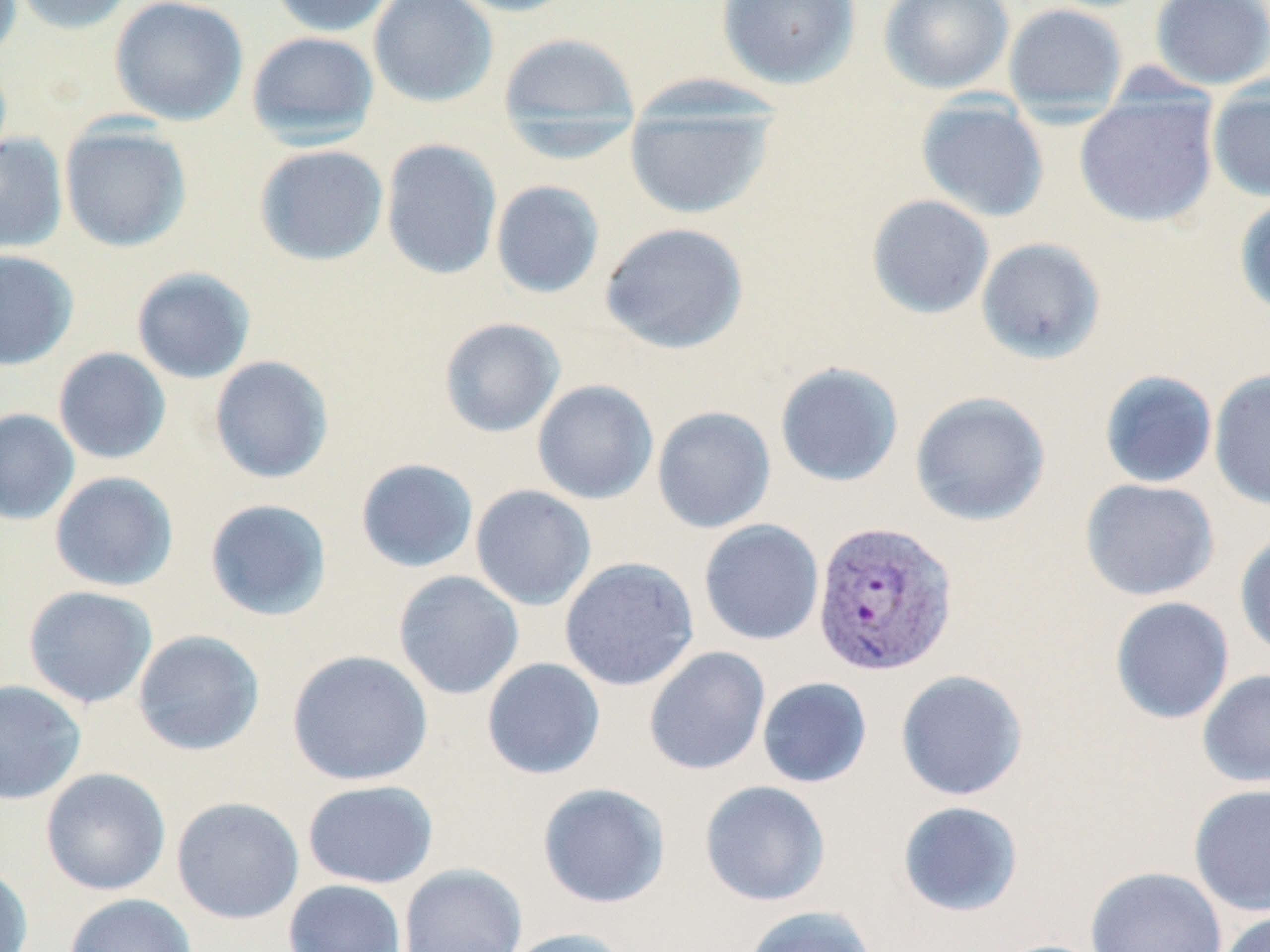

slide_level_diagnosis: Plasmodium vivax
stain: May-Grünwald-Giemsa
plasmodium_vivax_infected_red_blood_cell_locations: 'approximate bounding boxes as named x1/y1/x2/y2 corners in pixels: (x1=810, y1=520, x2=959, y2=676)'
magnification: 1000x
image_size: 1270×952 pixels
preparation: thin blood smear
modality: optical microscopy
field_of_view: single
uninfected_red_blood_cell_locations: 'approximate bounding boxes as named x1/y1/x2/y2 corners in pixels: (x1=10, y1=0, x2=135, y2=34), (x1=109, y1=0, x2=248, y2=126), (x1=268, y1=0, x2=397, y2=37), (x1=368, y1=0, x2=498, y2=108), (x1=444, y1=0, x2=583, y2=17), (x1=716, y1=0, x2=861, y2=89), (x1=878, y1=0, x2=1015, y2=94), (x1=1150, y1=0, x2=1270, y2=90), (x1=1003, y1=3, x2=1128, y2=116), (x1=497, y1=30, x2=640, y2=134), (x1=246, y1=31, x2=380, y2=148), (x1=1207, y1=81, x2=1270, y2=204), (x1=1074, y1=97, x2=1219, y2=228), (x1=915, y1=98, x2=1049, y2=223), (x1=624, y1=102, x2=778, y2=219), (x1=59, y1=122, x2=192, y2=252), (x1=0, y1=133, x2=68, y2=254), (x1=380, y1=138, x2=502, y2=280), (x1=254, y1=144, x2=389, y2=266), (x1=490, y1=180, x2=605, y2=299), (x1=866, y1=194, x2=995, y2=319), (x1=1234, y1=195, x2=1270, y2=318), (x1=599, y1=222, x2=749, y2=354), (x1=976, y1=237, x2=1106, y2=365), (x1=0, y1=249, x2=79, y2=371), (x1=131, y1=266, x2=256, y2=384), (x1=439, y1=317, x2=566, y2=438), (x1=53, y1=347, x2=171, y2=464), (x1=209, y1=355, x2=334, y2=484), (x1=774, y1=361, x2=904, y2=488), (x1=1208, y1=369, x2=1270, y2=511), (x1=1099, y1=370, x2=1218, y2=489), (x1=532, y1=379, x2=658, y2=505), (x1=909, y1=391, x2=1050, y2=526), (x1=651, y1=405, x2=776, y2=533), (x1=0, y1=408, x2=80, y2=525), (x1=355, y1=458, x2=479, y2=573), (x1=49, y1=471, x2=179, y2=592), (x1=1080, y1=478, x2=1220, y2=601), (x1=470, y1=485, x2=596, y2=610), (x1=204, y1=497, x2=333, y2=622), (x1=698, y1=518, x2=825, y2=645), (x1=1234, y1=531, x2=1270, y2=660), (x1=559, y1=556, x2=699, y2=691), (x1=393, y1=570, x2=524, y2=700), (x1=23, y1=585, x2=158, y2=708), (x1=1109, y1=596, x2=1235, y2=724), (x1=132, y1=630, x2=265, y2=756), (x1=643, y1=645, x2=771, y2=776), (x1=287, y1=649, x2=433, y2=786), (x1=482, y1=657, x2=606, y2=780), (x1=895, y1=669, x2=1028, y2=801), (x1=1197, y1=669, x2=1270, y2=790), (x1=757, y1=677, x2=872, y2=788), (x1=0, y1=679, x2=87, y2=805), (x1=40, y1=767, x2=171, y2=896), (x1=302, y1=780, x2=438, y2=888), (x1=699, y1=780, x2=831, y2=906), (x1=537, y1=782, x2=671, y2=909), (x1=1188, y1=783, x2=1270, y2=916), (x1=171, y1=796, x2=304, y2=925), (x1=897, y1=800, x2=1023, y2=917), (x1=397, y1=863, x2=528, y2=952), (x1=0, y1=864, x2=33, y2=952), (x1=1085, y1=865, x2=1228, y2=952), (x1=283, y1=879, x2=407, y2=952), (x1=64, y1=893, x2=198, y2=952), (x1=742, y1=905, x2=879, y2=952), (x1=1216, y1=910, x2=1270, y2=952), (x1=499, y1=927, x2=635, y2=952)'